Report the malaria status of this cell.
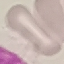

It is uninfected.

preparation = thin smear
image type = automatically extracted cell patch, resized to 64 × 64 pixels
capture = smartphone camera at the microscope eyepiece
stain = Giemsa